Comment on the morphology of the red blood cells.
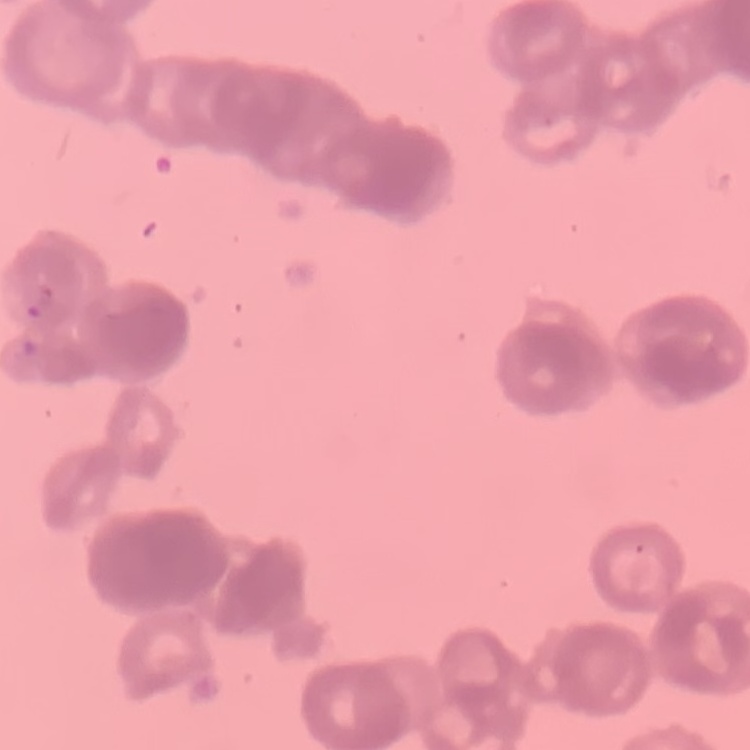

Rouleaux formation.

Summary:
  - Preparation: thin peripheral smear
  - Stain: Field's or Giemsa
  - Image type: square crop of a larger photomicrograph